Identify the parasite.
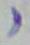

Toxoplasma gondii.

1000x magnification. Photomicrograph.